Outline each blood parasite and name the species.
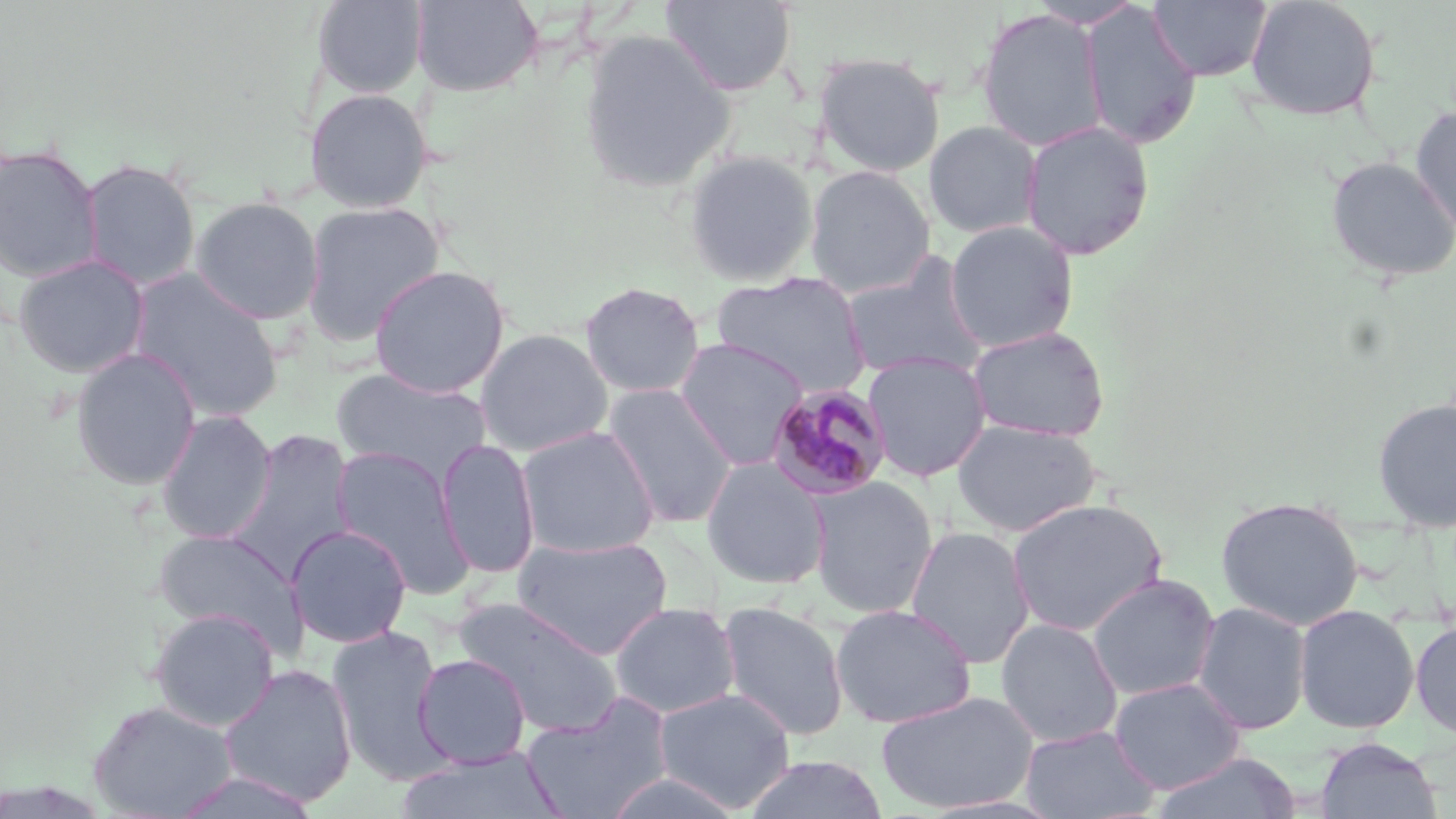
Approximate bounding boxes as (x1, y1, x2, y2) in pixels.
Plasmodium malariae-infected red blood cells: (767, 382, 894, 500).
No Plasmodium falciparum, Plasmodium ovale, Plasmodium vivax, Babesia divergens, or Trypanosoma brucei observed.

slide-level diagnosis = Plasmodium malariae
uninfected red blood cell locations = approximate bounding boxes as (x1, y1, x2, y2) in pixels: (311, 0, 428, 99), (411, 0, 543, 96), (1147, 0, 1273, 82), (1244, 0, 1383, 122), (661, 1, 797, 97), (1027, 1, 1146, 29), (1079, 3, 1202, 150), (975, 7, 1108, 152), (578, 28, 736, 194), (812, 51, 946, 178), (303, 87, 433, 213), (1409, 106, 1456, 241), (1019, 119, 1155, 260), (923, 121, 1043, 239), (0, 143, 103, 283), (683, 149, 819, 287), (1324, 156, 1456, 283), (80, 158, 201, 291), (804, 166, 935, 298), (189, 196, 324, 324), (300, 200, 445, 346), (944, 220, 1080, 352), (840, 252, 990, 383), (13, 254, 150, 378), (369, 264, 511, 398), (127, 269, 285, 422), (711, 271, 871, 396), (579, 281, 705, 399), (967, 325, 1111, 443), (475, 328, 614, 456), (674, 338, 811, 470), (70, 348, 202, 491), (862, 351, 992, 482), (331, 368, 494, 485), (602, 383, 739, 529), (1371, 397, 1456, 533), (155, 410, 277, 544), (951, 418, 1102, 536), (516, 426, 660, 559), (226, 429, 356, 580), (436, 439, 540, 579), (332, 446, 474, 596), (700, 457, 832, 590), (806, 476, 940, 618), (1216, 495, 1365, 630), (1006, 497, 1168, 637), (286, 524, 412, 648), (905, 525, 1035, 669), (153, 528, 304, 649), (512, 535, 674, 658), (1086, 573, 1220, 701), (451, 596, 625, 738), (609, 601, 740, 719), (717, 601, 850, 741), (1191, 601, 1312, 735), (831, 603, 977, 728), (1294, 604, 1420, 734), (148, 606, 280, 731), (995, 617, 1123, 748), (1410, 619, 1456, 739), (327, 625, 451, 783), (413, 653, 531, 768), (218, 664, 358, 807), (1109, 677, 1246, 794), (653, 687, 795, 812), (875, 689, 1039, 814), (520, 694, 674, 819), (87, 699, 238, 819), (1020, 725, 1160, 819), (1314, 737, 1443, 819), (395, 748, 565, 819), (1151, 751, 1304, 819), (740, 755, 890, 818), (168, 770, 324, 818)
magnification = 1000x
image size = 1456×819 pixels
preparation = thin blood smear
modality = optical microscopy
stain = May-Grünwald-Giemsa
field of view = one of a larger specimen